Assess this cell for malaria.
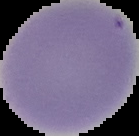
It is uninfected.

{
  "image_size": "139×136 pixels",
  "preparation": "thin blood smear",
  "image_type": "segmented cell region with the area outside set to black"
}